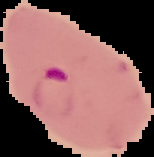
From a thin blood smear. The area outside the segmented cell region is set to black. Image is 154×157 pixels. Result: malaria parasites detected.